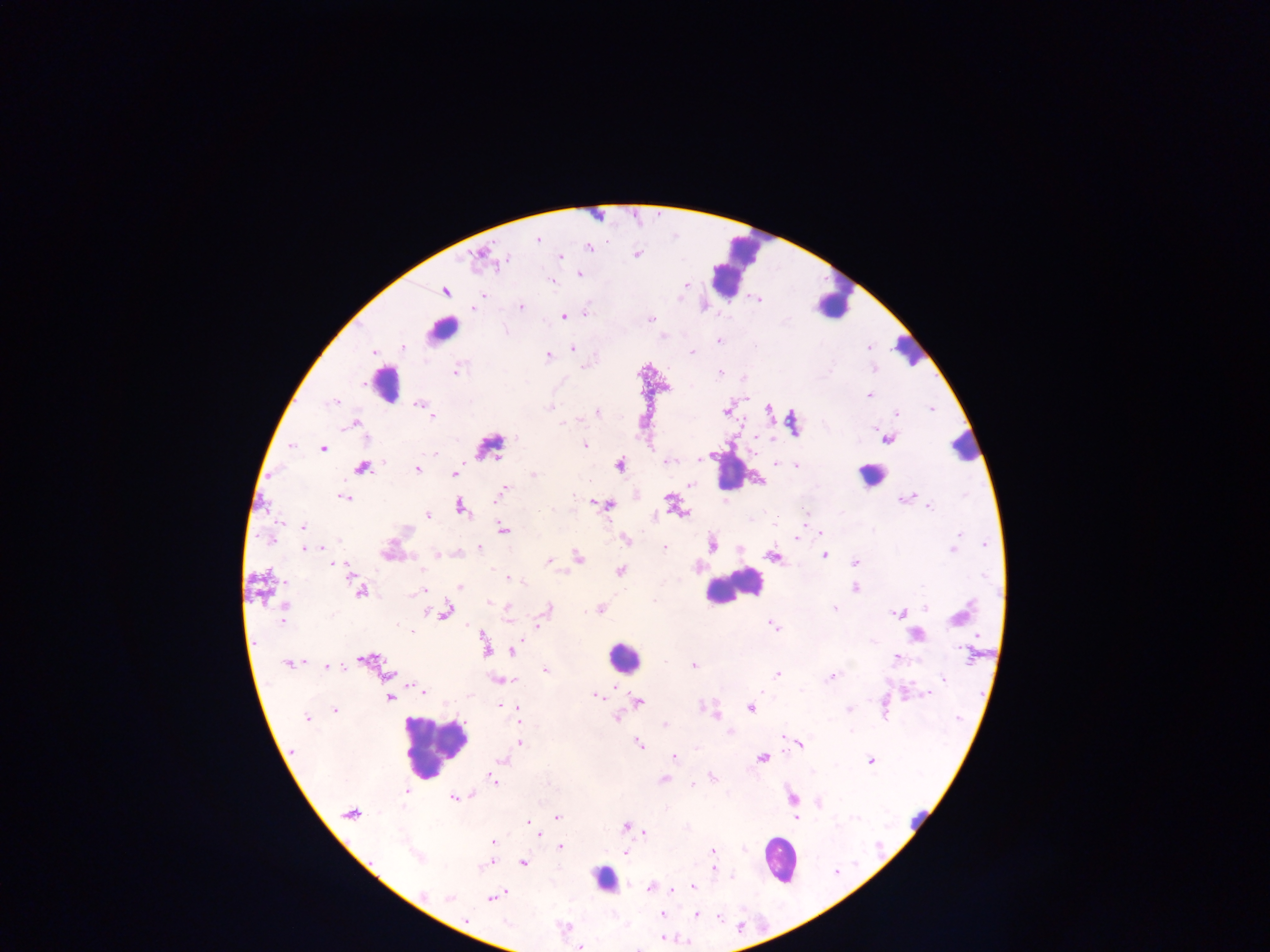

country: Ghana
capture: mobile-phone photograph through a microscope
plasmodium_parasite_locations: 'approximate centers as x y in pixels: 537 240; 589 247; 637 254; 478 256; 561 256; 505 260; 578 273; 551 281; 685 285; 445 291; 482 295; 759 299; 521 306; 474 307; 585 313; 564 316; 650 319; 506 331; 718 341; 403 347; 573 348; 868 348; 375 352; 692 352; 548 356; 582 367; 456 370; 720 373; 743 377; 868 395; 333 403; 419 404; 550 407; 769 409; 931 409; 726 411; 598 412; 896 413; 432 416; 561 423; 354 424; 517 437; 755 437; 888 439; 585 445; 291 446; 322 447; 435 453; 700 459; 667 461; 776 463; 619 466; 798 466; 362 468; 417 469; 454 474; 533 475; 759 481; 690 485; 505 487; 574 495; 343 498; 903 498; 669 500; 608 506; 929 506; 461 508; 682 513; 428 515; 656 515; 804 515; 774 524; 304 527; 504 529; 820 533; 958 536; 797 538; 626 539; 270 540; 339 540; 712 545; 985 545; 322 547; 479 547; 304 548; 315 548; 664 548; 953 549; 437 554; 824 556; 578 557; 774 557; 548 561; 855 562; 334 565; 341 565; 619 571; 510 578; 522 581; 460 587; 854 588; 360 591; 421 591; 488 602; 507 607; 924 607; 285 608; 549 608; 835 608; 600 609; 445 611; 898 614; 958 615; 282 620; 539 625; 773 625; 411 631; 517 644; 486 647; 514 650; 970 654; 896 658; 366 659; 288 664; 694 666; 327 667; 545 669; 387 674; 776 675; 832 676; 943 678; 509 680; 422 691; 761 691; 928 694; 596 696; 389 699; 638 702; 501 705; 750 707; 707 709; 334 710; 849 710; 518 712; 714 712; 307 717; 616 719; 519 720; 665 725; 730 732; 783 737; 520 743; 639 744; 799 745; 695 748; 674 757; 762 758; 503 761; 871 761; 712 777; 664 779; 493 780; 693 784; 407 792; 473 795; 454 798; 792 798; 819 803; 350 814; 557 817; 796 819; 526 821; 625 826; 645 833; 540 834; 493 842; 561 847; 712 850; 626 852; 417 857; 523 863; 485 866; 713 868; 693 887; 650 888; 672 889; 422 894; 450 897; 491 897; 662 914; 696 915; 720 918; 466 920; 663 938; 581 947'
image_size: 1270×952 pixels
leukocyte_locations: 'approximate centers as x y in pixels: 733 266; 834 301; 442 331; 908 349; 385 389; 964 445; 487 447; 728 470; 870 473; 732 587; 623 657; 435 746; 918 813; 778 860; 604 880'
preparation: thick blood film
field_of_view: single